State which parasite is depicted.
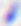

Toxoplasma gondii.

Summary:
  - Magnification: 400x
  - Modality: micrograph